Assess this cell for malaria.
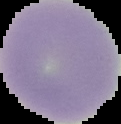
It is uninfected.

Summary:
  - Image type: segmented cell region with the area outside set to black
  - Image size: 121×124 pixels
  - Preparation: thin blood smear